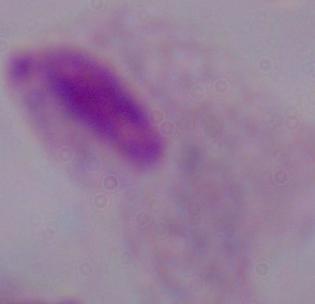

magnification = 1000x
identification = trichomonad
modality = micrograph